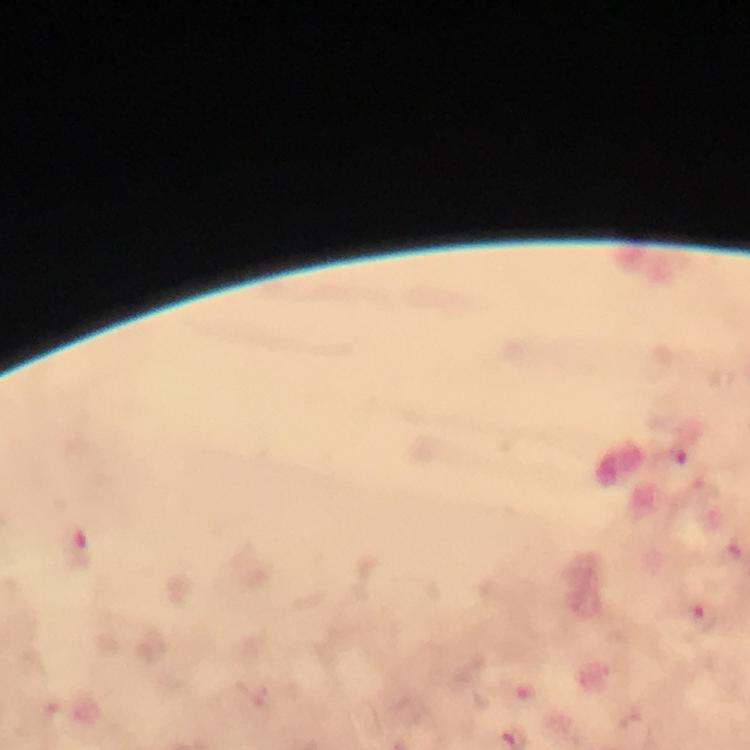

immersion oil = applied
capture = smartphone camera through the microscope
magnification = 100x
preparation = thick smear
cropped from = one field of view
malaria parasite locations = approximate centers as {x, y} in pixels: {679, 453}, {77, 547}, {704, 617}, {524, 691}, {629, 720}
image size = 750×750 pixels
context = from a diagnostic examination for malaria
stain = Giemsa